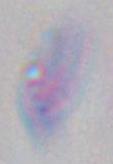

Summary:
  - Magnification: 1000x
  - Modality: micrograph
  - Identification: Toxoplasma gondii